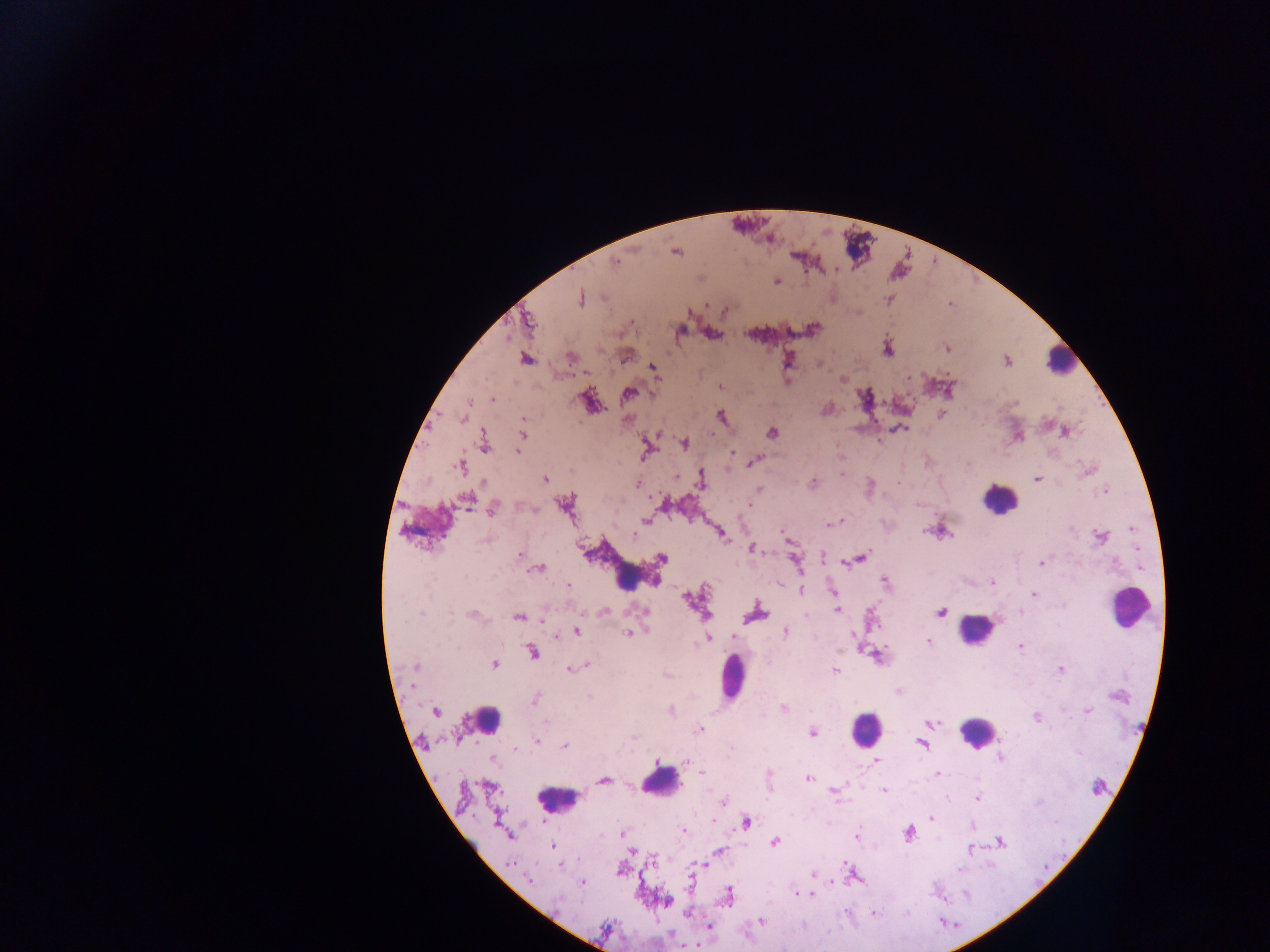

image_size: 1270×952 pixels
country: Ghana
plasmodium_parasite_locations: 'approximate centers as {x, y} in pixels (subset; some below the resolvable size): {676, 252}, {616, 262}, {777, 281}, {580, 299}, {706, 306}, {725, 311}, {529, 322}, {631, 322}, {823, 333}, {887, 350}, {948, 350}, {571, 357}, {526, 359}, {1007, 362}, {653, 368}, {909, 377}, {843, 379}, {719, 387}, {628, 394}, {493, 399}, {941, 414}, {721, 416}, {463, 418}, {524, 420}, {901, 428}, {1065, 432}, {772, 433}, {523, 435}, {684, 443}, {484, 445}, {647, 450}, {518, 452}, {733, 453}, {755, 460}, {460, 467}, {1087, 471}, {841, 474}, {676, 477}, {1037, 479}, {701, 481}, {483, 482}, {813, 483}, {636, 484}, {759, 490}, {1105, 491}, {467, 501}, {565, 505}, {492, 509}, {646, 521}, {839, 522}, {833, 523}, {1132, 529}, {926, 531}, {941, 531}, {634, 535}, {723, 535}, {1100, 537}, {485, 541}, {1137, 548}, {520, 556}, {824, 557}, {662, 558}, {862, 558}, {796, 561}, {851, 561}, {844, 563}, {1042, 564}, {540, 569}, {620, 572}, {654, 582}, {992, 582}, {885, 583}, {568, 586}, {801, 589}, {831, 590}, {1034, 595}, {687, 598}, {609, 604}, {836, 610}, {642, 611}, {940, 612}, {1020, 612}, {755, 613}, {421, 614}, {472, 614}, {519, 617}, {543, 619}, {576, 632}, {786, 632}, {854, 635}, {733, 636}, {556, 638}, {709, 638}, {928, 642}, {1021, 647}, {532, 653}, {494, 665}, {586, 665}, {415, 666}, {569, 669}, {1061, 670}, {835, 671}, {589, 697}, {535, 699}, {782, 707}, {1087, 711}, {435, 712}, {1036, 716}, {700, 720}, {546, 722}, {931, 723}, {813, 732}, {635, 737}, {537, 741}, {921, 744}, {564, 745}, {514, 750}, {1079, 752}, {999, 758}, {493, 759}, {876, 761}, {657, 762}, {687, 762}, {702, 773}, {938, 773}, {769, 774}, {808, 779}, {604, 780}, {838, 789}, {834, 791}, {884, 791}, {977, 799}, {723, 801}, {1039, 803}, {714, 816}, {931, 818}, {712, 821}, {746, 822}, {972, 826}, {684, 831}, {907, 833}, {621, 834}, {856, 836}, {1001, 842}, {775, 843}, {553, 846}, {971, 850}, {631, 851}, {719, 851}, {846, 862}, {700, 864}, {510, 865}, {960, 870}, {812, 874}, {529, 880}, {582, 883}, {831, 883}, {796, 893}, {811, 894}, {965, 894}, {729, 895}, {666, 901}, {845, 912}, {874, 913}, {687, 915}, {760, 921}, {709, 927}'
preparation: thick blood film
capture: mobile-phone photograph through a microscope
leukocyte_locations: 'approximate centers as {x, y} in pixels: {1060, 361}, {998, 499}, {1129, 607}, {976, 629}, {734, 677}, {487, 719}, {866, 727}, {977, 732}, {662, 784}, {556, 799}'
field_of_view: single